Locate every Plasmodium parasite.
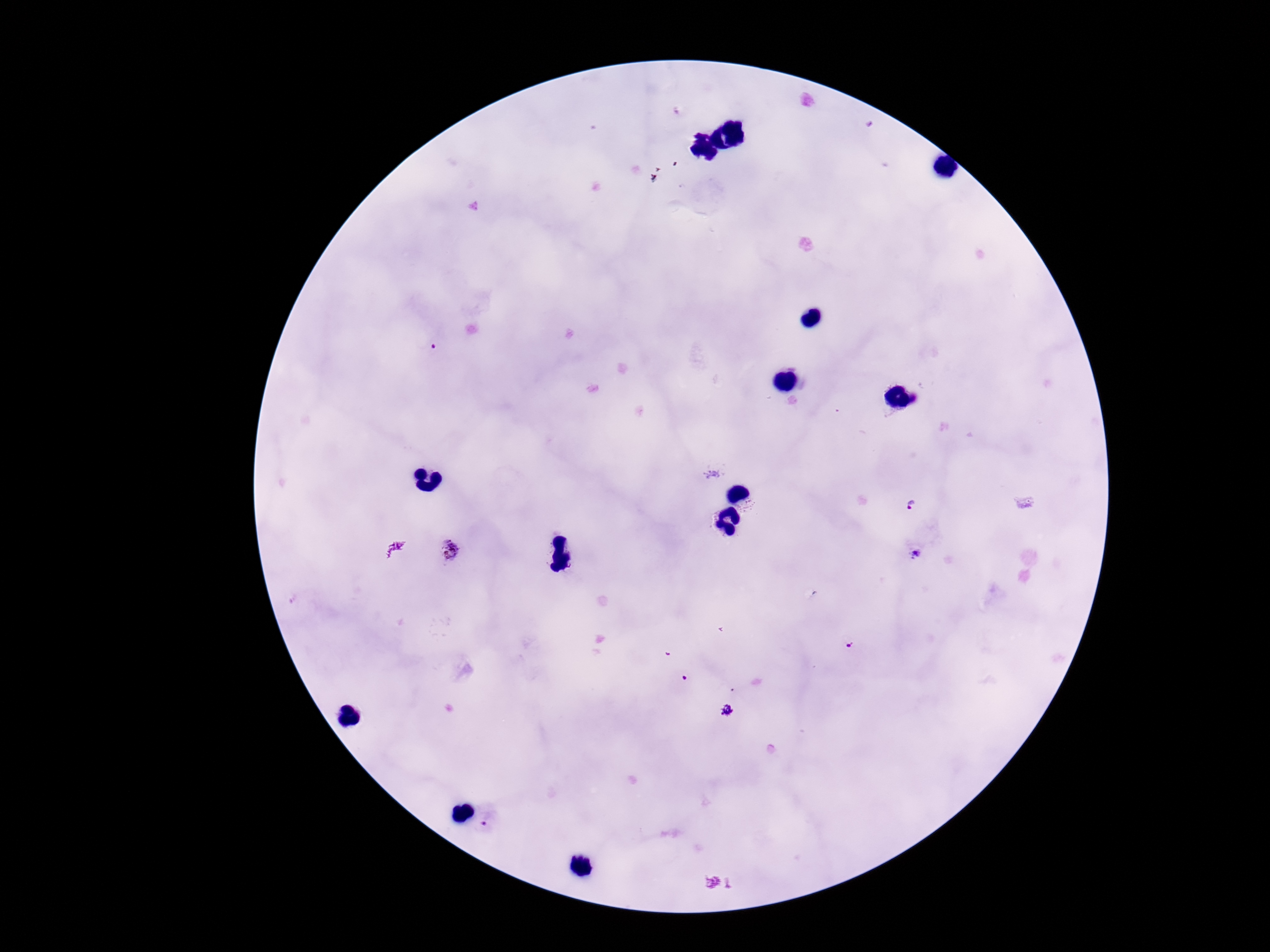

Approximate object centers, in pixels from the top-left corner.
Plasmodium parasites: (x=432, y=346), (x=913, y=506), (x=451, y=549), (x=916, y=555), (x=848, y=644), (x=688, y=677), (x=726, y=710), (x=486, y=822).

stain = Giemsa
field of view = one from this slide
capture = smartphone camera through the microscope eyepiece
preparation = thick peripheral-blood smear
patient malaria status = infected
magnification = 100x
image size = 1270×952 pixels